Classify this cell by malaria status.
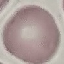
Uninfected.

Summary:
  - Stain: Giemsa
  - Capture: smartphone camera at the microscope eyepiece
  - Preparation: thin blood film
  - Image type: cell patch, automatically extracted from a larger field of view and resized to 64 × 64 pixels